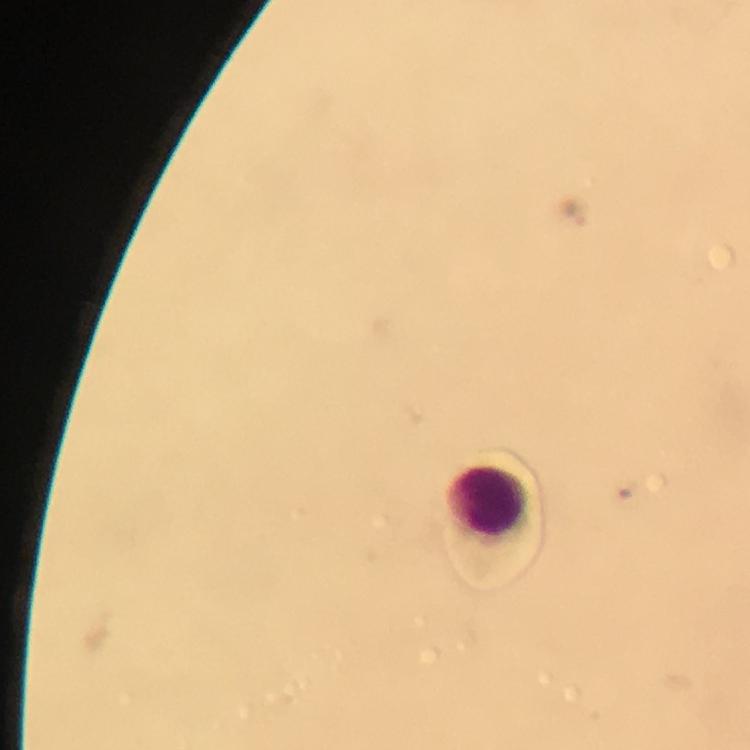

Approximate centers as [x, y] in pixels. Leukocyte locations: [486, 503]. Plasmodium parasite locations: [572, 216]. 100x magnification. Image is 750×750 pixels. Smartphone photograph taken through a microscope. From a diagnostic examination for malaria. Giemsa stain. Thick smear. Immersion oil was used. A crop from one field of view.